Assess the morphology of the erythrocytes.
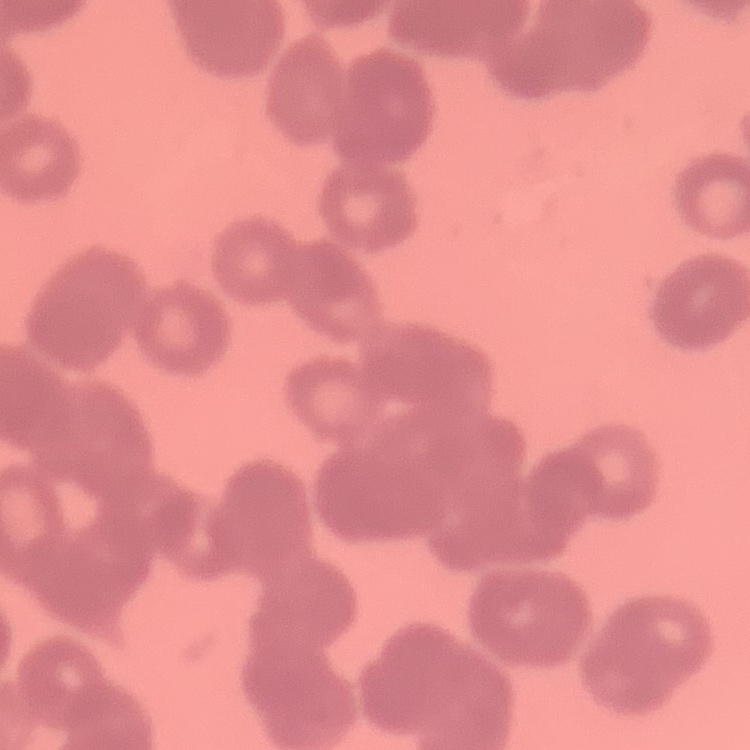
Rouleaux formation.

Square crop of a larger photomicrograph. Thin blood film. Stained with either Field's or Giemsa.